Report the malaria status of this cell.
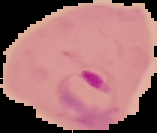
Parasitized.

image_size: 157×133 pixels
image_type: segmented cell region on a black background
preparation: thin blood smear